Evaluate for parasitized red blood cells.
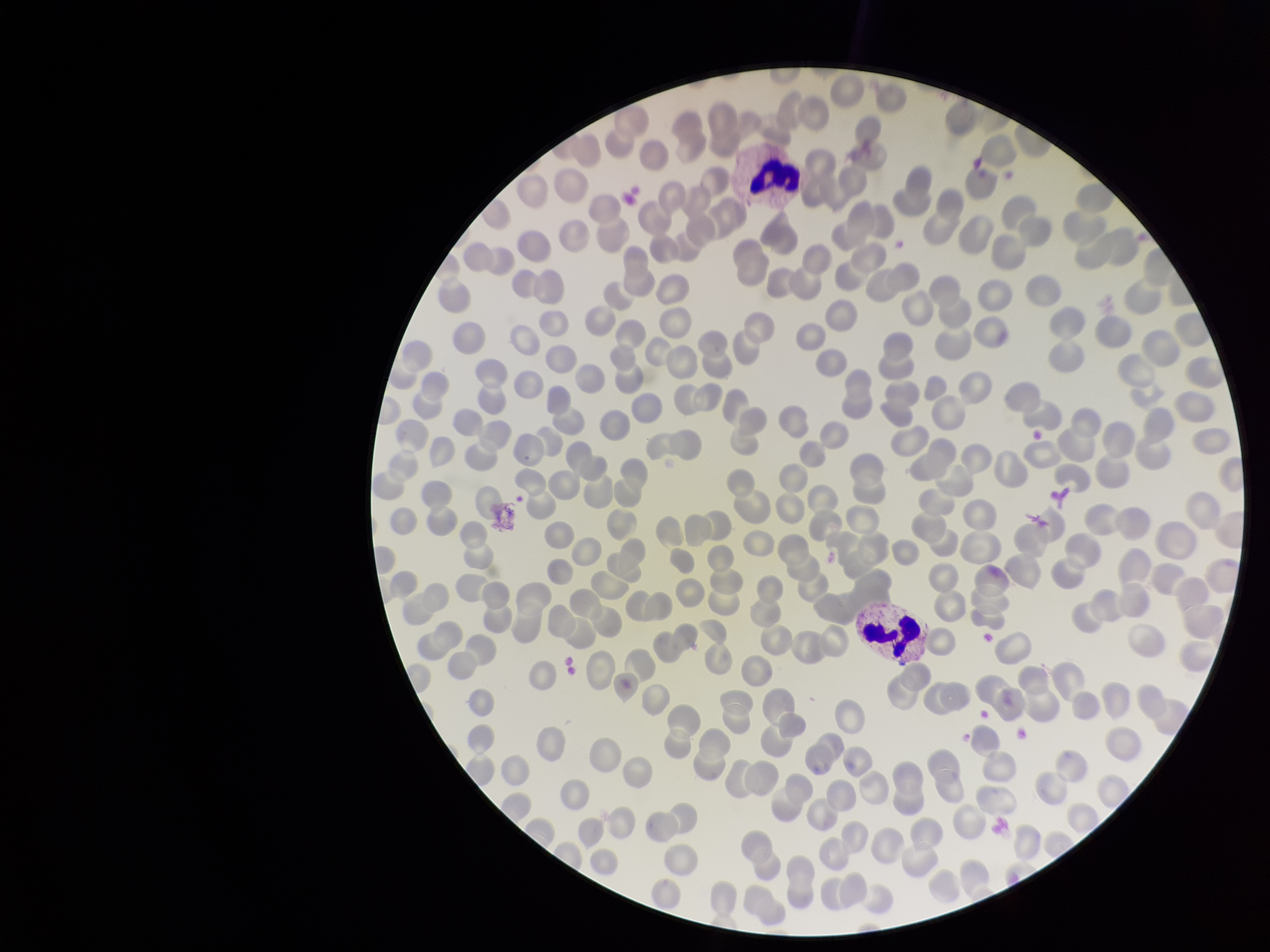

None identified.

Photographed through the microscope eyepiece with a smartphone camera. Parasitized red blood cell count: 0. Patient malaria status: negative. Stained with Giemsa. Red blood cell count: 291. Preparation: thin smear. Image is 1270×952 pixels. Single field of view.